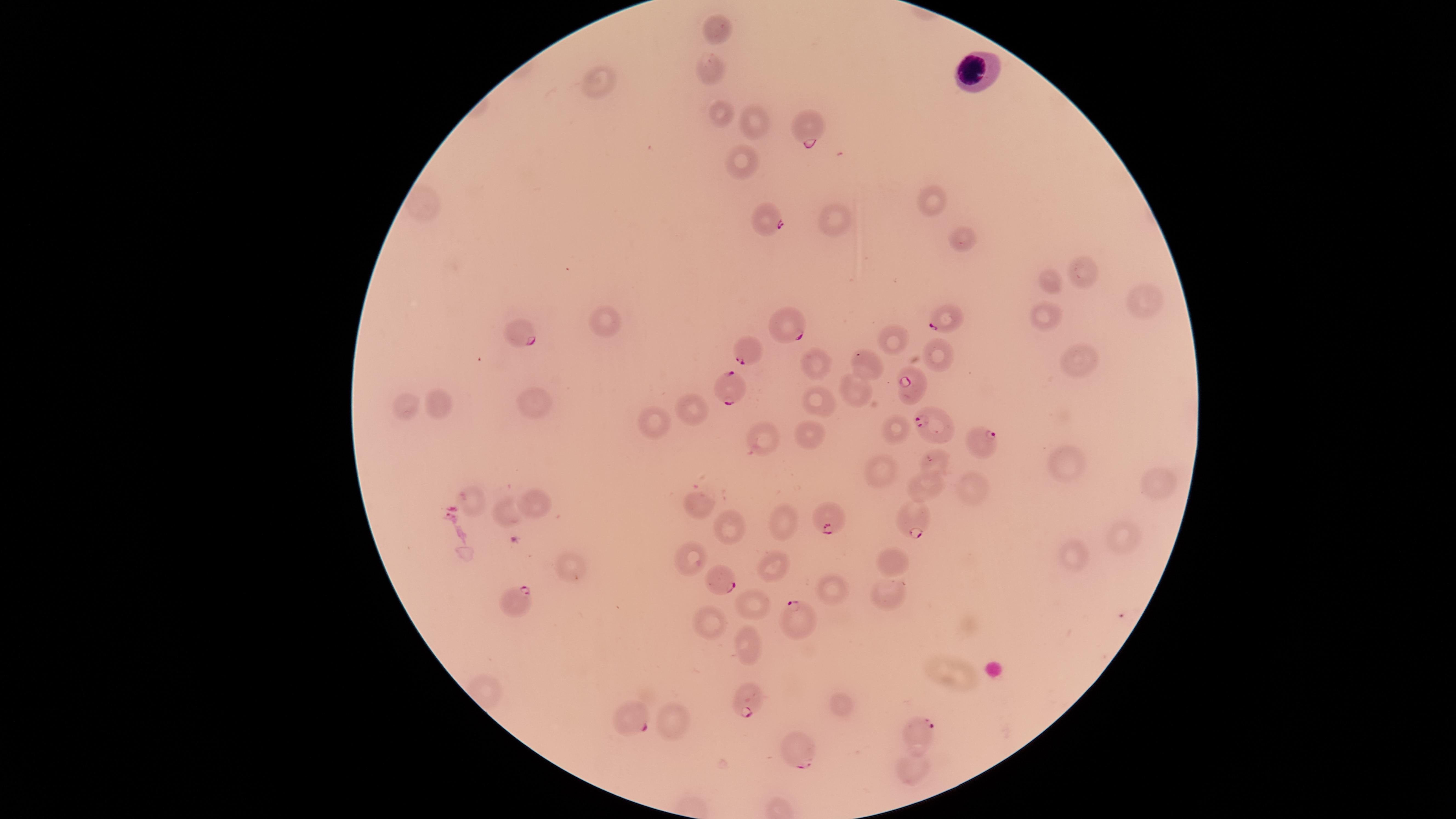
Approximate marker points as [x, y] in pixels. WBCs: [976, 70]. Parasitized RBCs: [808, 130], [765, 221], [937, 319], [794, 327], [523, 333], [748, 352], [908, 386], [734, 387], [928, 422], [986, 440], [823, 519], [913, 522], [720, 579], [516, 602], [802, 617], [745, 701], [634, 716], [919, 729], [802, 748]. Uninfected RBCs: [717, 28], [711, 64], [597, 80], [718, 112], [749, 123], [736, 162], [929, 199], [837, 227], [960, 234], [1085, 271], [1050, 281], [1144, 300], [1046, 318], [603, 322], [897, 338], [937, 352], [1081, 359], [871, 361], [815, 366], [856, 390], [818, 395], [534, 396], [438, 401], [408, 402], [696, 405], [892, 423], [643, 426], [812, 435], [752, 437], [881, 461], [934, 465], [1066, 465], [1158, 481], [926, 488], [973, 491], [471, 498], [534, 501], [702, 506], [506, 513], [783, 524], [730, 528], [1122, 536], [693, 556], [891, 557], [1073, 558], [565, 570], [772, 570], [829, 588], [886, 591], [751, 602], [710, 621], [748, 646], [839, 706], [669, 721], [912, 765]. Photographed with a smartphone camera through the microscope eyepiece. Single field of view. Image is 1456×819 pixels. Giemsa stain. The visible region is circular. Species: Plasmodium falciparum. Presence: malaria parasites seen. Thin smear of blood.